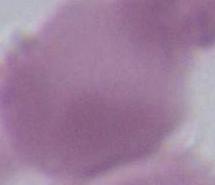

1000x magnification. Micrograph. An erythrocyte is seen.